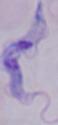
Summary:
  - Magnification: 1000x
  - Modality: photomicrograph
  - Identification: trypanosome